Assess this cell for malaria.
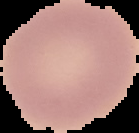
It is uninfected.

Image is 139×133 pixels. From a thin blood smear. Segmented cell region on a black background.